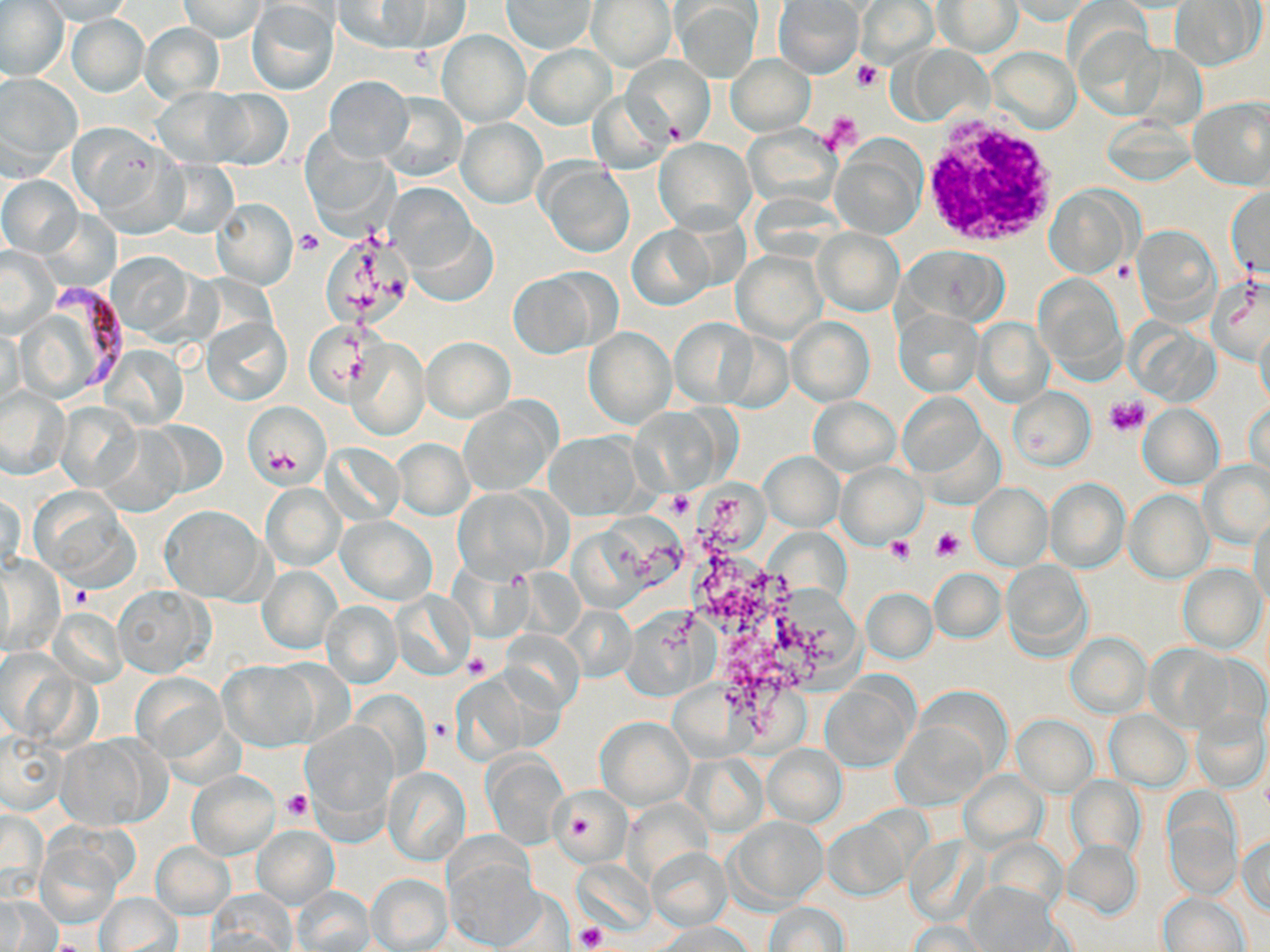
Summary:
  - Coordinate format: approximate bounding boxes as (x1,y1)-(x2,y2) corner pairs in pixels
  - White blood cell locations: (914,112)-(1061,249)
  - Uninfected red blood cell locations: (35,0)-(139,23), (179,0)-(266,42), (586,0)-(676,70), (774,0)-(864,77), (247,1)-(338,95), (334,1)-(431,52), (392,1)-(473,51), (501,1)-(596,53), (856,1)-(938,68), (934,1)-(1022,56), (1006,1)-(1103,23), (1172,1)-(1262,70), (0,3)-(68,80), (674,3)-(762,81), (67,15)-(147,95), (138,23)-(225,105), (1074,25)-(1164,120), (437,29)-(530,126), (524,44)-(616,130), (899,44)-(994,126), (987,47)-(1080,135), (622,54)-(713,142), (724,54)-(815,135), (0,73)-(82,176), (325,75)-(413,163), (153,87)-(254,167), (202,88)-(293,167), (587,90)-(673,174), (378,91)-(465,182), (1189,98)-(1270,190), (457,119)-(545,207), (68,122)-(176,223), (742,126)-(841,209), (654,138)-(754,232), (831,139)-(927,238), (538,160)-(635,258), (1,176)-(82,256), (389,183)-(478,276), (1227,186)-(1269,282), (1046,187)-(1139,278), (211,199)-(297,289), (409,218)-(497,307), (627,226)-(714,310), (1132,227)-(1220,318), (813,228)-(903,316), (0,246)-(60,337), (903,247)-(1010,325), (732,250)-(826,343), (105,252)-(201,340), (507,271)-(603,358), (1036,273)-(1125,373), (1208,276)-(1269,365), (894,310)-(981,396), (201,317)-(292,406), (669,317)-(759,407), (786,317)-(874,406), (974,319)-(1053,407), (1255,321)-(1269,412), (305,323)-(369,404), (583,328)-(675,428), (717,331)-(794,412), (421,336)-(515,421), (348,339)-(428,438), (100,343)-(188,430), (0,387)-(69,477), (1009,388)-(1094,470), (897,393)-(986,477), (808,397)-(899,475), (1248,397)-(1269,482), (460,398)-(559,494), (56,401)-(143,493), (244,402)-(329,488), (1138,405)-(1222,489), (145,420)-(228,499), (95,424)-(185,517), (543,433)-(644,517), (392,438)-(472,518), (323,443)-(404,525), (759,452)-(844,530), (1200,461)-(1270,548), (836,464)-(925,548), (1044,479)-(1130,573), (261,483)-(344,570), (968,484)-(1052,570), (30,488)-(137,588), (454,488)-(558,579), (1123,489)-(1213,584), (1,490)-(24,574), (159,506)-(269,604), (1250,514)-(1270,612), (338,516)-(436,604), (0,555)-(64,656), (1000,559)-(1092,661), (1178,563)-(1267,653), (258,565)-(340,654), (929,568)-(1005,642), (114,586)-(212,677), (862,587)-(937,664), (391,590)-(474,678), (321,600)-(402,689), (566,604)-(636,683), (501,628)-(585,714), (1065,632)-(1150,718), (1145,644)-(1234,731), (219,659)-(319,751), (133,673)-(226,761), (821,678)-(915,773), (1104,709)-(1192,791), (1190,709)-(1269,794), (1013,715)-(1097,796), (894,716)-(994,810), (596,717)-(692,808), (302,721)-(397,830), (0,733)-(65,815), (56,735)-(160,829), (763,744)-(846,826), (482,750)-(568,849), (384,767)-(470,864), (188,770)-(279,859), (959,770)-(1046,851), (1067,775)-(1145,857), (549,785)-(630,866), (1163,798)-(1241,898), (1,805)-(44,902), (729,815)-(826,908), (824,816)-(915,902), (252,826)-(338,908), (36,831)-(126,927), (1239,834)-(1270,915), (1061,838)-(1141,919), (151,842)-(234,919), (646,847)-(732,930), (444,856)-(547,947), (366,873)-(452,951), (964,882)-(1060,950), (292,887)-(374,951), (208,893)-(296,951), (95,894)-(181,952), (1159,894)-(1249,952), (1,896)-(59,949), (764,901)-(849,951), (657,922)-(752,952), (907,924)-(988,951)
  - Platelet locations: (853,59)-(883,92), (823,112)-(863,153), (663,121)-(685,144), (295,229)-(322,257), (1104,396)-(1149,436), (667,491)-(691,516), (931,527)-(965,561), (886,536)-(915,565), (71,585)-(94,610), (463,653)-(494,680), (282,789)-(312,821), (572,818)-(594,838), (574,925)-(607,952), (52,937)-(88,952)
  - Plasmodium falciparum-infected red blood cell locations: (50,279)-(128,394)
  - Slide-level diagnosis: Plasmodium falciparum
  - Magnification: 1000x
  - Preparation: thin blood smear
  - Stain: May-Grünwald-Giemsa
  - Image size: 1270×952 pixels
  - Field of view: single
  - Modality: optical microscopy